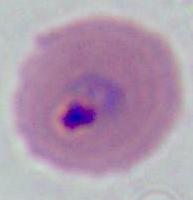
{
  "modality": "photomicrograph",
  "identification": "Plasmodium",
  "magnification": "400x or 1000x"
}